Identify the cell.
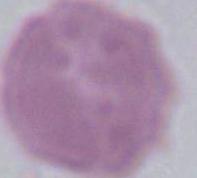
An erythrocyte.

{
  "magnification": "1000x",
  "modality": "photomicrograph"
}